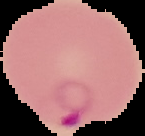

From a thin blood film. Cell region segmented out of the field of view; the surrounding area is masked to black. Image is 145×136 pixels. Malaria status: parasitized.